Outline each Plasmodium falciparum-infected red blood cell.
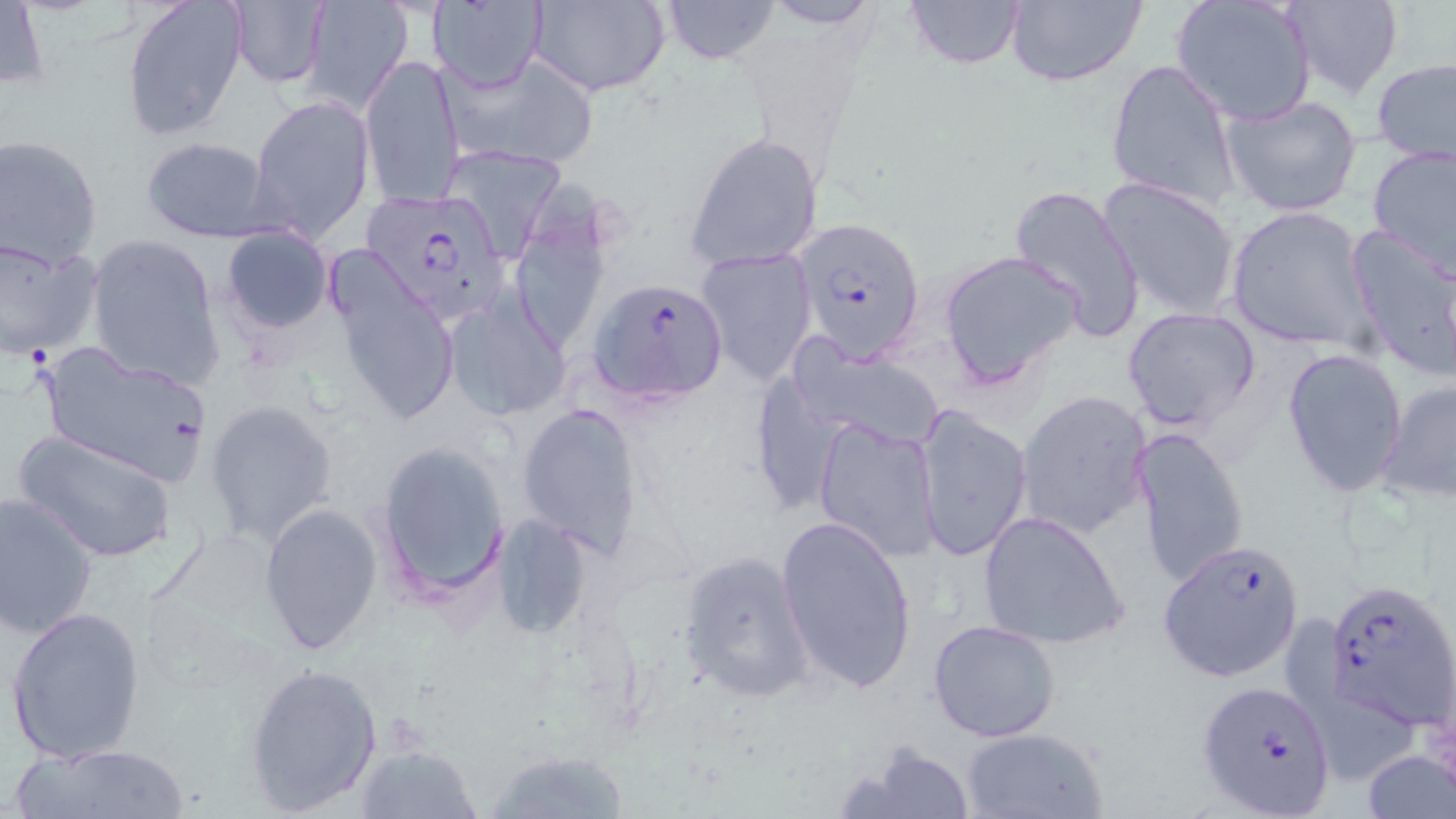

Approximate bounding boxes as [x1, y1, x2, y2] in pixels.
Plasmodium falciparum-infected red blood cells: [370, 200, 519, 331], [791, 216, 926, 362], [591, 279, 730, 404], [1158, 541, 1303, 680], [1320, 579, 1456, 729], [1195, 681, 1337, 816].

Summary:
  - Uninfected red blood cell locations: [120, 0, 247, 145], [298, 0, 414, 114], [662, 0, 780, 65], [902, 0, 1026, 68], [1005, 0, 1148, 88], [1170, 0, 1317, 125], [1278, 0, 1403, 100], [226, 1, 330, 88], [427, 1, 547, 90], [528, 1, 670, 96], [758, 1, 887, 29], [2, 2, 48, 92], [447, 52, 600, 170], [359, 54, 465, 209], [1372, 57, 1456, 165], [1105, 58, 1240, 209], [1219, 92, 1362, 218], [248, 94, 375, 241], [683, 132, 824, 274], [0, 135, 103, 269], [140, 137, 277, 242], [1367, 143, 1456, 278], [439, 144, 565, 262], [519, 172, 622, 355], [1096, 175, 1243, 321], [1009, 183, 1147, 341], [1226, 205, 1376, 353], [220, 226, 334, 334], [1344, 226, 1455, 380], [85, 234, 223, 388], [0, 239, 102, 358], [696, 246, 818, 385], [323, 248, 461, 429], [937, 249, 1084, 389], [442, 294, 572, 421], [1121, 305, 1260, 432], [789, 340, 946, 450], [37, 342, 215, 484], [1280, 345, 1407, 498], [1378, 378, 1456, 502], [1015, 388, 1154, 542], [204, 399, 339, 547], [516, 403, 645, 557], [913, 403, 1034, 563], [812, 417, 943, 562], [1131, 425, 1252, 593], [14, 427, 179, 564], [370, 441, 512, 604], [0, 490, 99, 639], [258, 501, 383, 655], [977, 510, 1131, 651], [489, 512, 595, 642], [774, 515, 919, 693], [677, 548, 816, 704], [1282, 602, 1418, 783], [4, 603, 147, 766], [927, 618, 1062, 743], [244, 661, 384, 815], [958, 727, 1108, 818], [844, 739, 975, 819], [11, 741, 194, 819], [1362, 744, 1454, 818], [355, 745, 483, 818], [485, 749, 634, 819]
  - Slide-level diagnosis: Plasmodium falciparum
  - Modality: light microscopy
  - Field of view: one of a larger specimen
  - Stain: May-Grünwald-Giemsa
  - Preparation: thin blood smear
  - Image size: 1456×819 pixels
  - Magnification: 1000x